State which parasite is depicted.
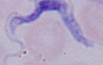
A trypanosome.

Captured at 1000x magnification. Micrograph.